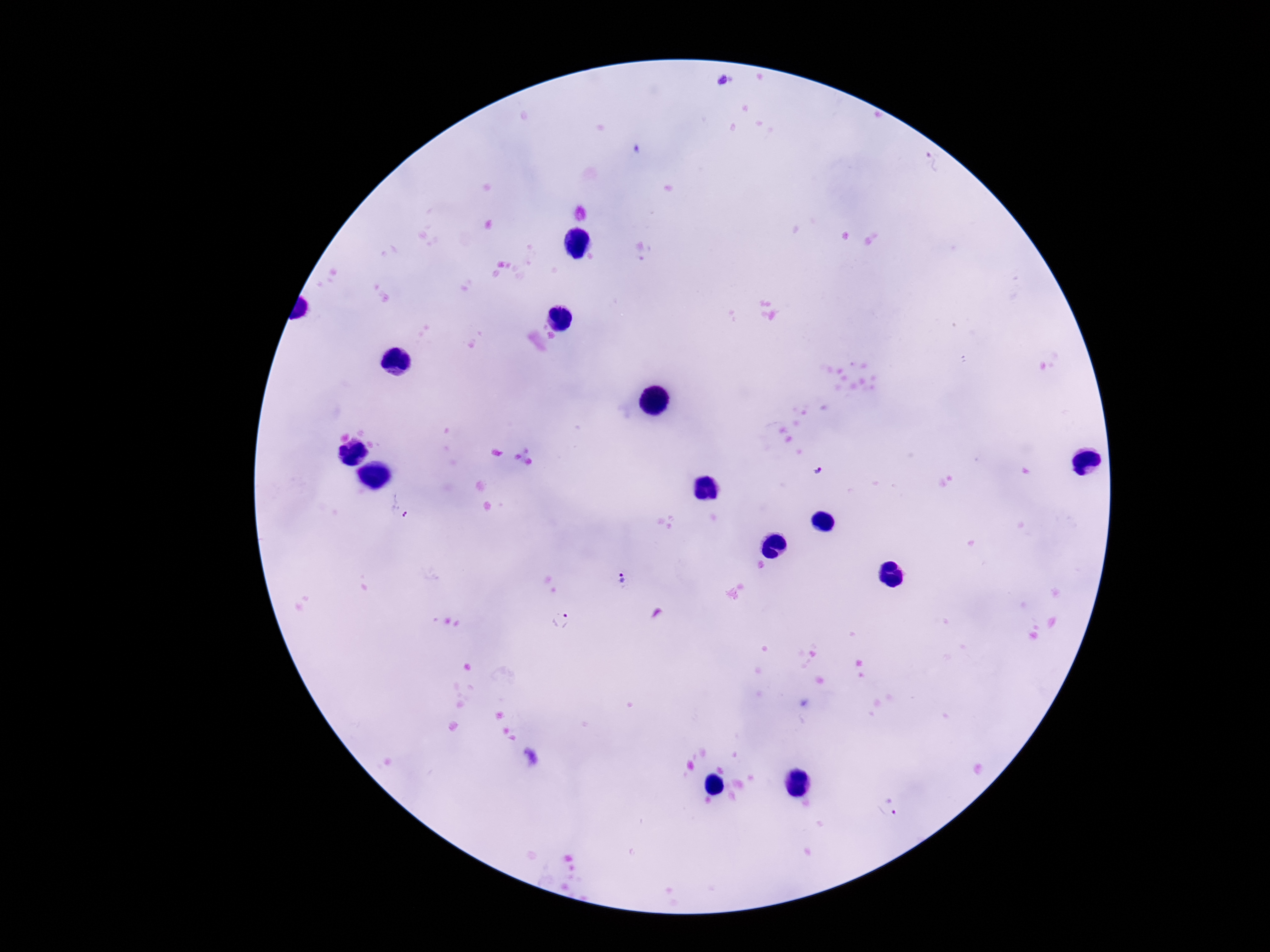

Approximate centers as [x, y] in pixels. Plasmodium parasite locations: [721, 81], [932, 162], [818, 471], [397, 507], [623, 580], [559, 619], [885, 807]. Photographed through the microscope eyepiece with a smartphone camera. Image is 1270×952 pixels. Patient malaria status: positive. Giemsa-stained preparation. 100x magnification. Thick peripheral-blood smear. One field from this slide.